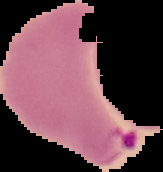 Malaria status: parasitized. From a thin blood film. Cell region segmented out of the field of view; the surrounding area is masked to black. Image is 163×172 pixels.